Outline each Plasmodium falciparum-infected red blood cell.
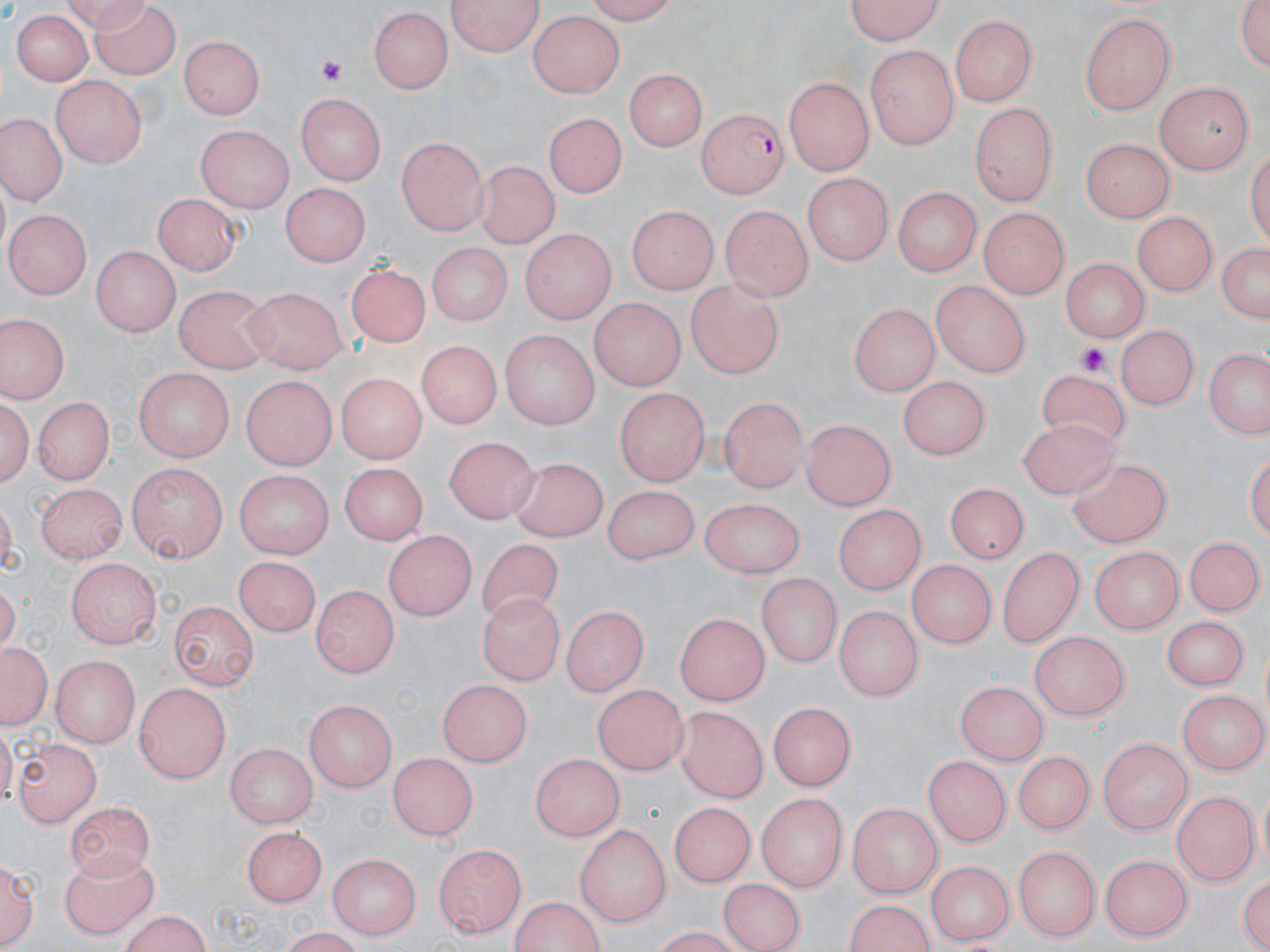

Approximate bounding boxes as (x1,y1)-(x2,y2) corner pairs in pixels.
Plasmodium falciparum-infected red blood cells: (696,106)-(787,199).

Summary:
  - Platelet locations: (312,54)-(349,85), (1075,342)-(1116,377)
  - Uninfected red blood cell locations: (446,0)-(546,58), (573,0)-(686,24), (839,0)-(948,43), (1232,0)-(1270,73), (88,2)-(182,77), (367,8)-(454,95), (7,11)-(97,89), (527,12)-(623,98), (1081,14)-(1176,115), (950,15)-(1036,108), (180,36)-(266,121), (865,42)-(959,151), (625,67)-(709,152), (51,74)-(146,169), (782,75)-(875,176), (1153,80)-(1258,173), (297,93)-(386,186), (968,102)-(1062,205), (543,111)-(628,200), (0,113)-(64,202), (197,125)-(291,212), (825,128)-(918,221), (395,135)-(489,233), (1080,138)-(1175,223), (477,159)-(557,248), (282,185)-(366,271), (895,188)-(978,277), (153,193)-(237,277), (624,206)-(716,296), (718,206)-(810,302), (979,206)-(1071,299), (8,208)-(91,299), (1133,208)-(1219,294), (519,228)-(613,322), (1215,237)-(1268,327), (423,240)-(514,327), (93,248)-(176,338), (1056,257)-(1151,339), (343,262)-(430,349), (684,280)-(786,384), (931,280)-(1030,376), (174,285)-(275,374), (242,287)-(348,377), (586,297)-(683,391), (847,304)-(936,395), (0,312)-(69,402), (1117,325)-(1199,414), (497,331)-(599,430), (417,342)-(497,432), (1205,344)-(1270,439), (133,366)-(237,458), (1035,368)-(1138,457), (334,371)-(431,463), (901,375)-(990,458), (240,376)-(335,473), (613,384)-(710,485), (1,391)-(37,493), (718,393)-(808,493), (33,394)-(114,482), (800,417)-(897,509), (1016,417)-(1119,498), (441,438)-(536,524), (511,457)-(608,538), (333,460)-(427,540), (1066,460)-(1173,552), (128,462)-(229,564), (233,466)-(338,556), (942,482)-(1032,563), (37,484)-(129,560), (601,485)-(705,565), (698,499)-(808,578), (834,504)-(924,597), (384,527)-(475,623), (1189,534)-(1261,618), (475,538)-(564,626), (995,544)-(1085,647), (1087,544)-(1186,631), (235,556)-(321,635), (908,556)-(995,649), (69,557)-(161,646), (755,573)-(842,667), (313,584)-(396,680), (479,591)-(566,685), (170,598)-(256,689), (833,606)-(923,698), (560,607)-(650,695), (674,610)-(770,705), (1164,617)-(1247,691), (1029,629)-(1130,721), (2,643)-(50,728), (52,654)-(140,746), (438,679)-(530,769), (954,681)-(1053,763), (133,682)-(231,781), (593,684)-(688,775), (1179,689)-(1265,777), (305,700)-(397,794), (678,702)-(769,800), (768,702)-(858,790), (1099,735)-(1196,834), (12,737)-(98,824), (226,742)-(318,828), (1011,752)-(1098,834), (387,754)-(478,839), (533,754)-(624,842), (925,755)-(1010,849), (1173,789)-(1257,886), (755,793)-(850,887), (66,799)-(154,881), (668,802)-(757,889), (848,803)-(942,900), (573,824)-(674,924), (243,828)-(324,906), (432,840)-(524,935), (1014,844)-(1101,941), (61,849)-(158,937), (327,851)-(421,937), (1102,851)-(1197,938), (1,854)-(39,951), (925,861)-(1016,943), (1236,868)-(1270,952), (720,877)-(804,952), (503,896)-(610,952), (847,902)-(936,952), (116,912)-(214,951)
  - Slide-level diagnosis: Plasmodium falciparum
  - Image size: 1270×952 pixels
  - Stain: May-Grünwald-Giemsa
  - Modality: light microscopy
  - Magnification: 1000x
  - Preparation: thin blood film
  - Field of view: single